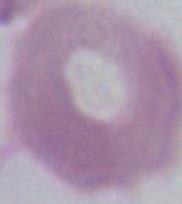
An erythrocyte is seen. Micrograph. 1000x magnification.